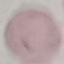
Summary:
  - Malaria status: uninfected
  - Image type: automatically extracted cell patch, resized to 64 × 64 pixels
  - Stain: Giemsa
  - Capture: smartphone through the microscope eyepiece
  - Preparation: thin blood smear